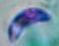

Summary:
  - Modality: photomicrograph
  - Magnification: 1000x
  - Identification: Toxoplasma gondii